Name the parasite shown.
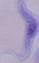
This is a trypanosome.

Captured at 1000x magnification. Photomicrograph.